Classify this cell by malaria status.
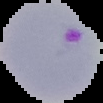

Parasitized.

Summary:
  - Image size: 103×103 pixels
  - Image type: segmented cell region on a black background
  - Preparation: thin blood smear